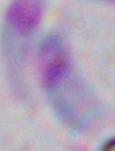 Captured at 1000x magnification. Toxoplasma gondii is seen. Photomicrograph.